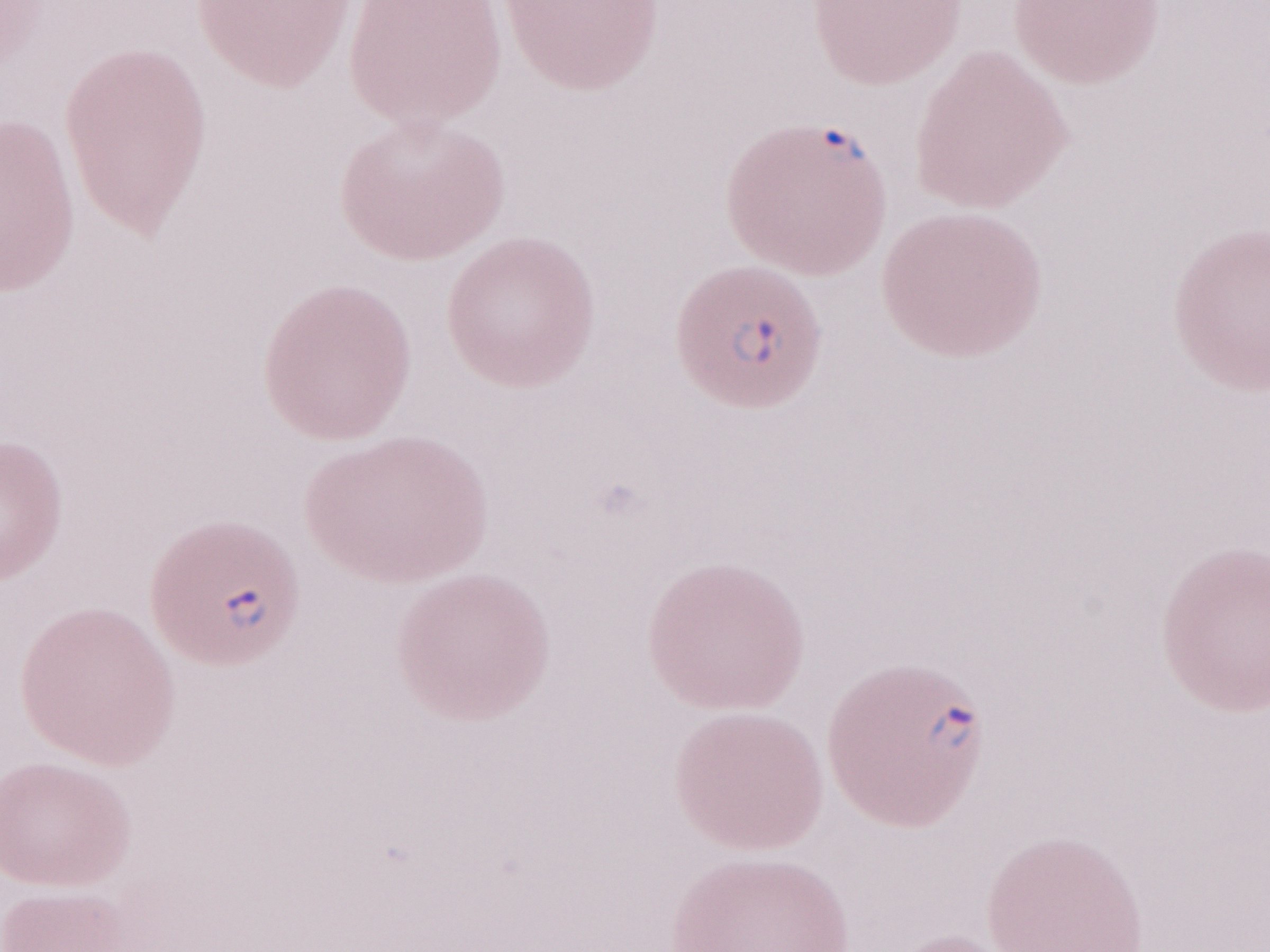
Single field of view. May-Grünwald-Giemsa (MGG) stain. Thin peripheral-blood smear. Patient diagnosis: malaria infection. Image is 1270×952 pixels. Magnification: 1,000x. Olympus BX43 microscope and DP73 digital camera.